Point out each leukocyte.
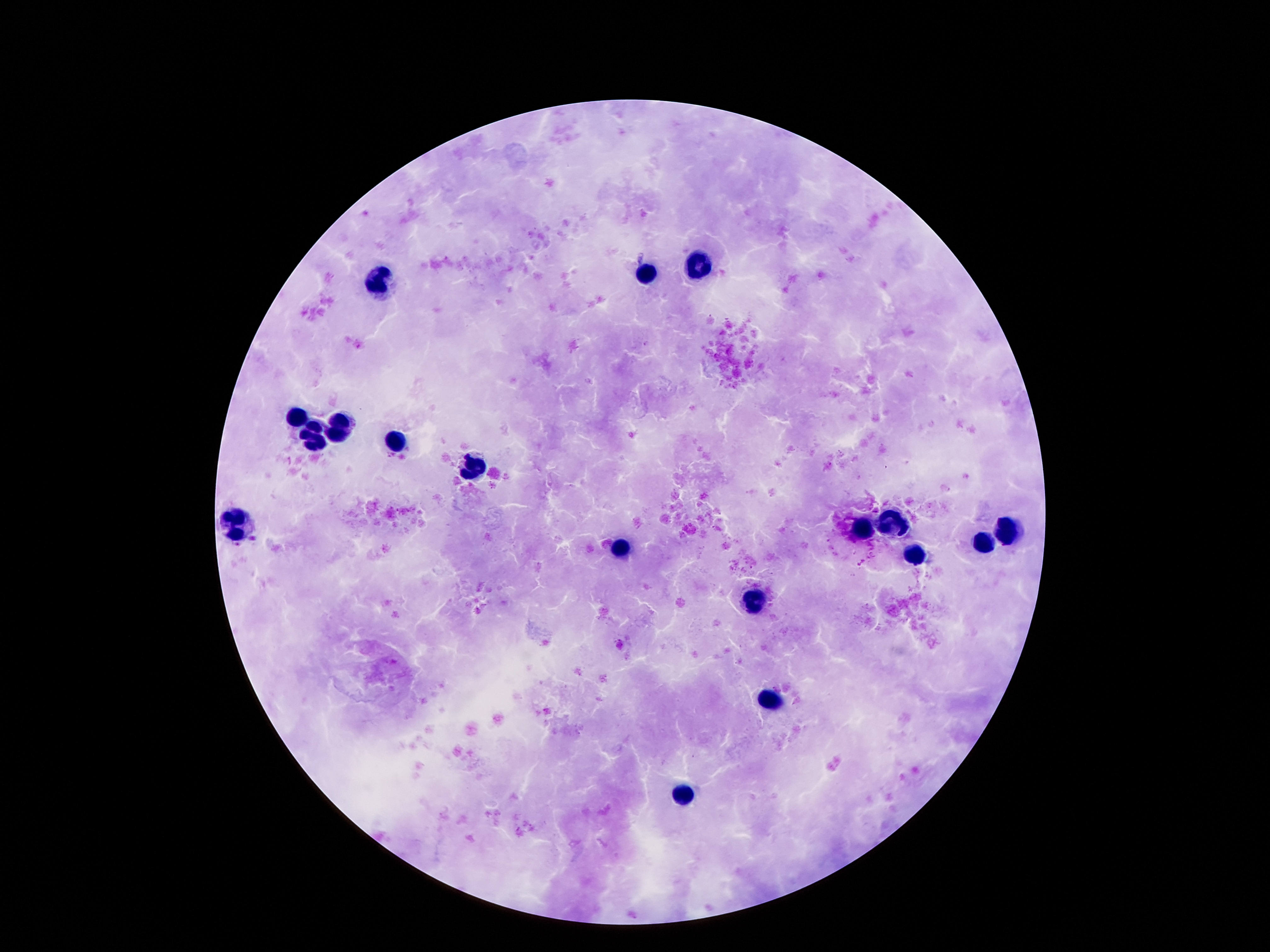
Approximate centers as [x, y] in pixels.
Leukocytes: [701, 262], [646, 277], [380, 282], [294, 417], [340, 424], [313, 436], [393, 446], [470, 469], [237, 522], [896, 522], [1010, 527], [865, 528], [985, 543], [617, 552], [917, 555], [756, 603], [770, 700], [686, 793].

Giemsa-stained preparation. Single field of view. Image is 1270×952 pixels. Thick peripheral-blood smear. Photographed through the microscope eyepiece with a smartphone camera. 100x magnification. Patient malaria status: uninfected.